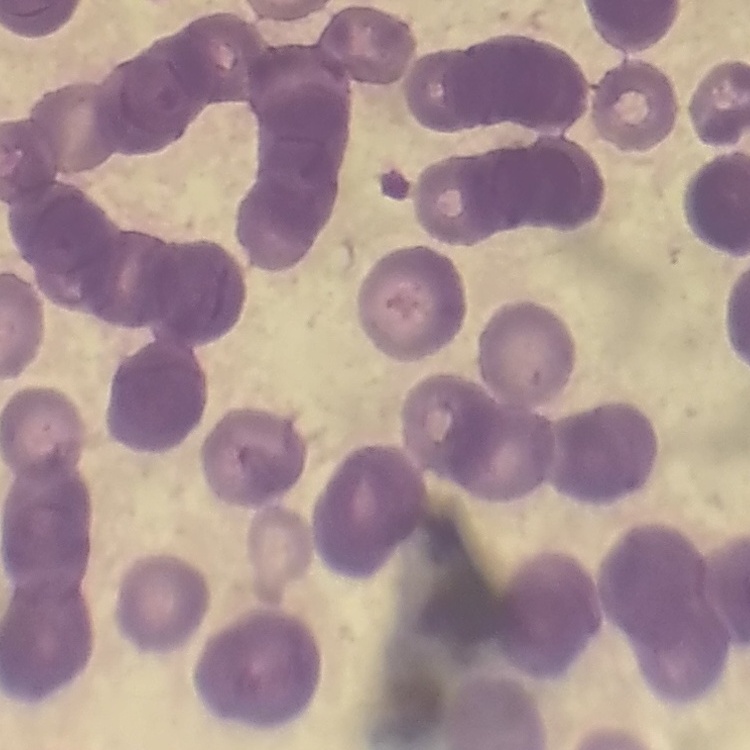

Summary:
  - Red blood cell morphology: rouleaux formation
  - Stain: Field's or Giemsa
  - Image type: one tile cut from a larger photomicrograph
  - Preparation: thin peripheral smear